Outline each blood parasite and name the species.
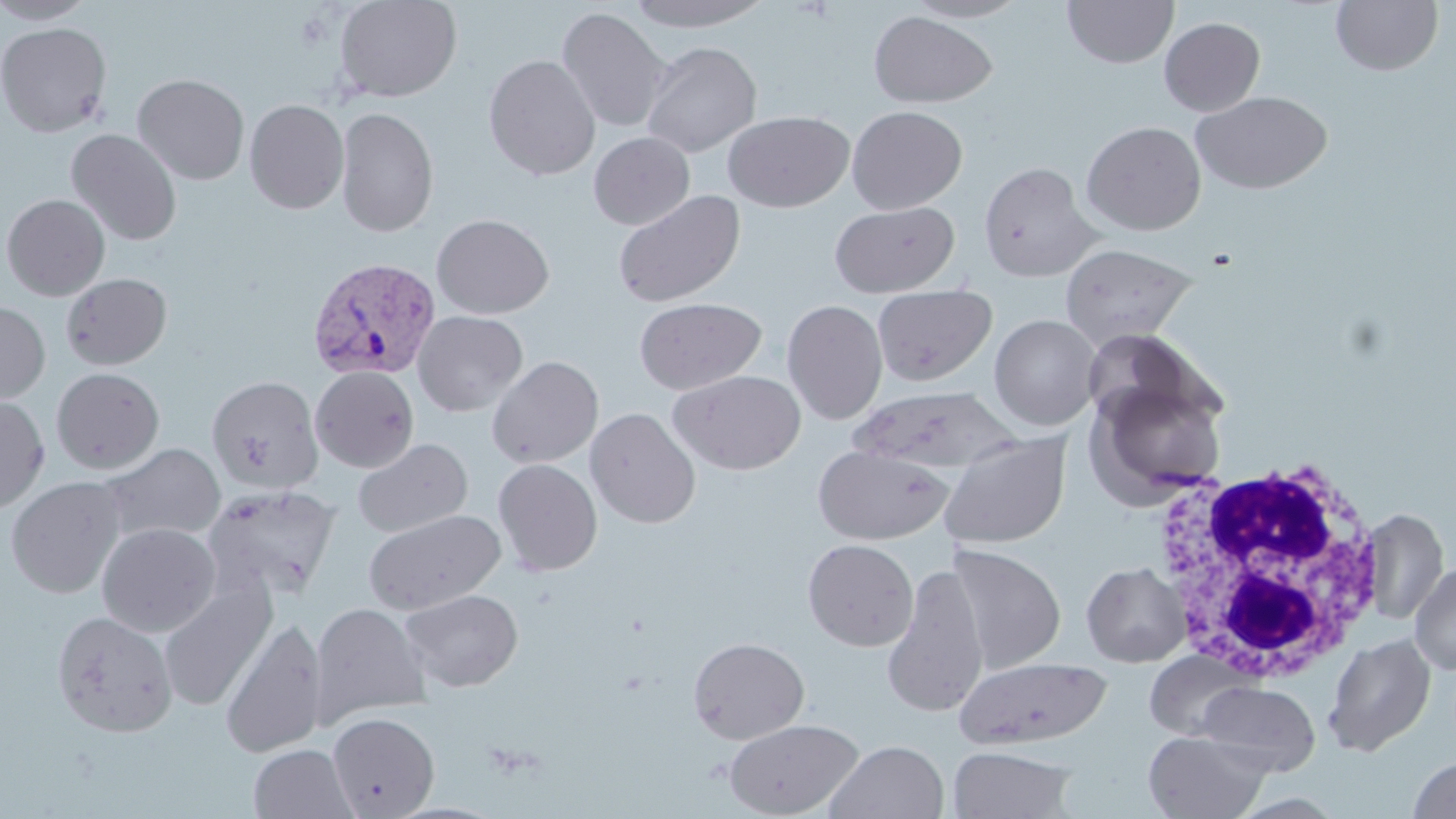

Approximate bounding boxes as (x1, y1, x2, y2) in pixels.
Plasmodium vivax-infected red blood cells: (308, 257, 440, 381).
No Plasmodium falciparum, Plasmodium ovale, Plasmodium malariae, Babesia divergens, or Trypanosoma brucei observed.

{
  "slide_level_diagnosis": "Plasmodium vivax",
  "uninfected_red_blood_cell_locations": "approximate bounding boxes as (x1, y1, x2, y2) in pixels: (0, 0, 97, 25), (333, 0, 463, 103), (624, 0, 774, 32), (903, 0, 1031, 22), (1063, 0, 1178, 69), (1331, 0, 1444, 76), (556, 6, 671, 132), (868, 11, 998, 108), (1159, 17, 1265, 117), (0, 22, 112, 138), (641, 41, 762, 158), (483, 54, 601, 180), (132, 73, 250, 185), (1192, 90, 1332, 194), (244, 99, 349, 214), (847, 105, 967, 214), (335, 106, 439, 237), (722, 110, 854, 212), (1081, 121, 1206, 235), (66, 128, 182, 246), (589, 132, 695, 230), (978, 161, 1101, 282), (613, 189, 745, 308), (1, 193, 110, 300), (829, 200, 959, 297), (431, 214, 554, 319), (1060, 242, 1196, 349), (61, 272, 172, 370), (872, 284, 996, 386), (634, 297, 767, 394), (782, 299, 887, 425), (0, 300, 51, 405), (412, 310, 528, 416), (989, 314, 1101, 430), (1078, 327, 1208, 428), (486, 355, 604, 468), (310, 366, 419, 472), (51, 367, 164, 474), (670, 370, 806, 475), (206, 374, 324, 494), (1086, 376, 1228, 506), (850, 387, 1018, 475), (0, 394, 49, 512), (585, 407, 701, 529), (937, 431, 1071, 549), (353, 438, 472, 538), (98, 443, 225, 544), (812, 444, 952, 545), (493, 458, 603, 576), (5, 477, 125, 598), (201, 484, 341, 602), (1360, 508, 1449, 626), (363, 509, 505, 614), (97, 522, 220, 637), (802, 538, 919, 651), (946, 545, 1066, 673), (1081, 561, 1190, 666), (1409, 561, 1456, 675), (881, 563, 990, 718), (158, 579, 276, 711), (399, 588, 523, 692), (309, 602, 430, 726), (52, 610, 178, 737), (220, 618, 328, 758), (1323, 633, 1436, 757), (688, 637, 810, 744), (1144, 649, 1253, 741), (955, 656, 1111, 749), (1196, 680, 1320, 775), (327, 711, 439, 817), (723, 717, 864, 818), (1144, 730, 1270, 818), (825, 740, 949, 819), (249, 744, 358, 819), (947, 745, 1076, 819), (1407, 756, 1456, 818)",
  "stain": "May-Grünwald-Giemsa",
  "preparation": "thin blood smear",
  "white_blood_cell_locations": "approximate bounding boxes as (x1, y1, x2, y2) in pixels: (1149, 457, 1393, 683)",
  "image_size": "1456×819 pixels",
  "field_of_view": "single",
  "modality": "light microscopy",
  "magnification": "1000x"
}